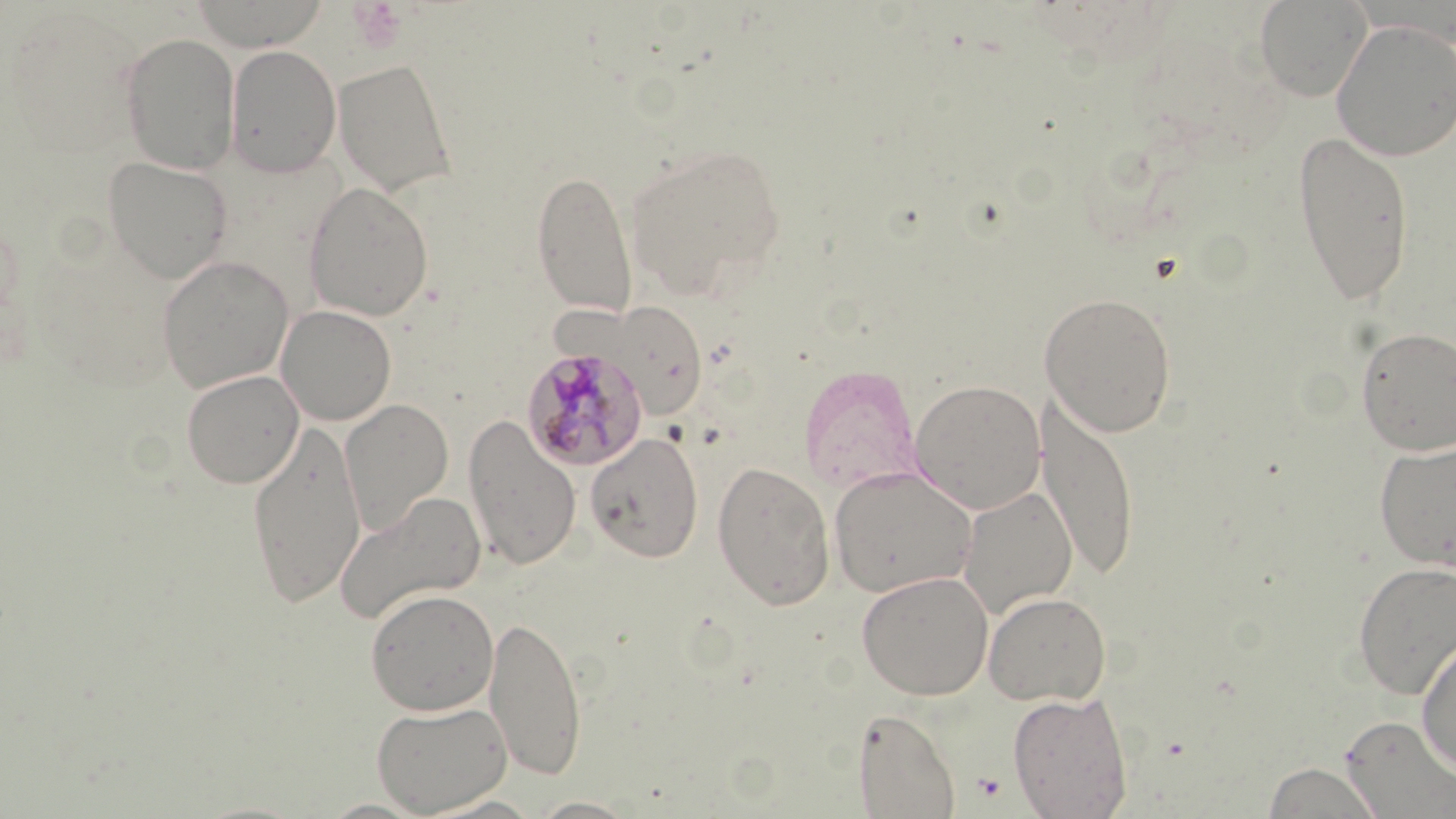

slide_level_diagnosis: Plasmodium malariae
modality: optical microscopy
preparation: thin blood smear
field_of_view: single
image_size: 1456×819 pixels
magnification: 1000x
uninfected_red_blood_cell_locations: 'approximate bounding boxes as [x1, y1, x2, y2] in pixels: [190, 0, 329, 51], [1254, 0, 1371, 101], [1330, 19, 1456, 161], [119, 32, 241, 174], [226, 44, 342, 177], [332, 57, 459, 197], [1292, 129, 1415, 308], [623, 141, 787, 299], [102, 155, 234, 284], [531, 169, 638, 319], [303, 181, 435, 321], [157, 255, 294, 393], [1039, 291, 1178, 437], [593, 301, 710, 419], [276, 304, 396, 425], [1354, 325, 1456, 456], [799, 365, 923, 491], [181, 370, 304, 488], [909, 379, 1047, 515], [1037, 392, 1139, 580], [340, 399, 453, 536], [463, 414, 581, 572], [247, 417, 367, 608], [585, 432, 703, 563], [1372, 436, 1456, 572], [712, 460, 835, 610], [828, 466, 978, 598], [957, 486, 1078, 618], [334, 490, 487, 624], [1352, 561, 1456, 699], [856, 570, 994, 700], [365, 588, 499, 716], [983, 590, 1112, 706], [485, 613, 587, 781], [1416, 635, 1456, 775], [1007, 690, 1133, 818], [370, 700, 513, 815], [852, 708, 962, 818], [1339, 716, 1456, 816], [1260, 761, 1386, 818], [525, 796, 644, 818]'
plasmodium_malariae_infected_red_blood_cell_locations: 'approximate bounding boxes as [x1, y1, x2, y2] in pixels: [522, 346, 648, 470]'
stain: May-Grünwald-Giemsa